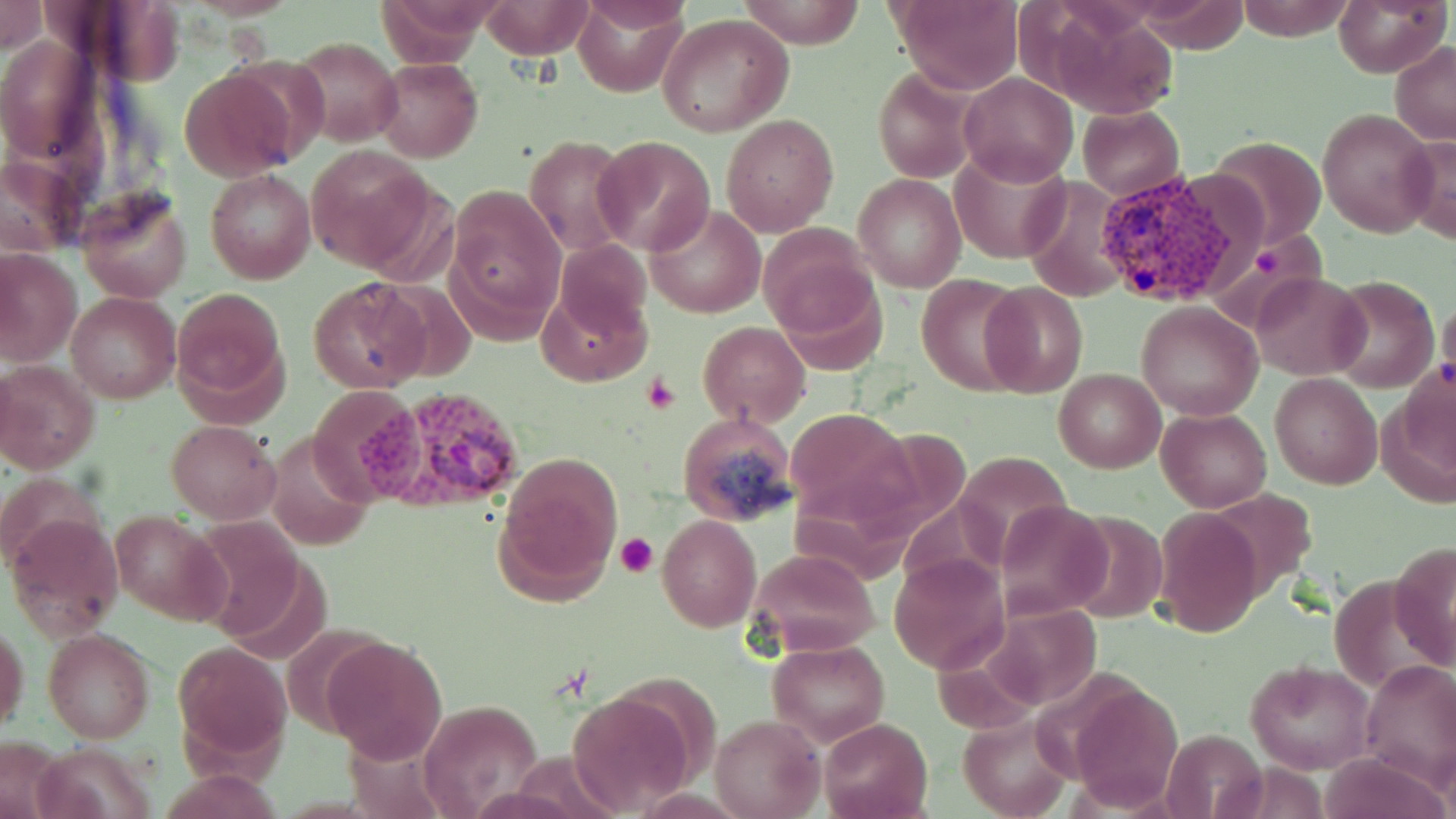

Approximate bounding boxes as (x1, y1, x2, y2) in pixels. Uninfected red blood cell locations: (0, 0, 45, 54), (573, 0, 688, 97), (736, 0, 865, 48), (893, 0, 1024, 94), (1135, 0, 1250, 52), (1236, 0, 1356, 41), (1333, 0, 1447, 76), (480, 1, 595, 59), (576, 2, 692, 37), (1043, 7, 1179, 118), (657, 15, 791, 138), (289, 35, 400, 147), (1390, 40, 1456, 144), (373, 57, 483, 162), (179, 67, 299, 182), (873, 67, 980, 183), (958, 73, 1077, 187), (1078, 105, 1184, 200), (1318, 107, 1438, 236), (721, 114, 839, 235), (524, 134, 631, 256), (1208, 134, 1327, 248), (1399, 135, 1456, 244), (592, 136, 714, 257), (949, 145, 1073, 265), (306, 148, 436, 273), (0, 155, 82, 256), (205, 169, 316, 284), (854, 173, 966, 293), (1020, 177, 1129, 301), (77, 188, 193, 302), (448, 188, 564, 326), (644, 204, 765, 318), (759, 227, 879, 342), (555, 241, 653, 342), (0, 248, 82, 365), (770, 267, 888, 378), (1251, 272, 1368, 379), (916, 274, 1026, 396), (1326, 275, 1439, 392), (308, 278, 431, 392), (538, 282, 650, 385), (981, 282, 1088, 398), (170, 286, 289, 413), (66, 292, 180, 404), (1438, 295, 1456, 395), (1136, 302, 1263, 420), (698, 322, 810, 427), (0, 361, 100, 473), (1054, 369, 1165, 473), (1269, 373, 1382, 490), (1156, 407, 1272, 511), (785, 409, 910, 524), (677, 412, 796, 526), (167, 420, 280, 522), (949, 451, 1079, 564), (495, 456, 620, 602), (1, 470, 99, 569), (994, 500, 1112, 619), (1154, 507, 1261, 639), (111, 509, 228, 625), (5, 511, 124, 639), (657, 515, 761, 632), (1390, 540, 1456, 671), (745, 548, 879, 658), (889, 555, 1010, 674), (980, 604, 1102, 713), (1, 623, 29, 736), (43, 628, 156, 744), (325, 637, 448, 763), (173, 639, 291, 766), (768, 641, 889, 745), (1360, 658, 1455, 787), (1244, 661, 1375, 775), (1070, 683, 1184, 812), (565, 688, 697, 815), (417, 699, 544, 818), (958, 713, 1073, 819), (713, 715, 824, 819), (819, 718, 933, 819), (1161, 729, 1267, 819), (0, 736, 68, 818), (161, 769, 285, 819). Plasmodium vivax-infected red blood cell locations: (1090, 165, 1234, 309), (357, 388, 526, 515). Platelet locations: (1255, 249, 1283, 281), (642, 372, 680, 415), (615, 531, 661, 578). Slide-level diagnosis: Plasmodium vivax. May-Grünwald-Giemsa stain. 1000x magnification. Optical microscopy. Image is 1456×819 pixels. Thin blood smear. One field of a larger specimen.